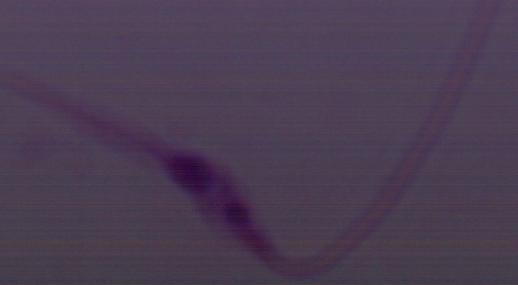

1000x magnification. Micrograph. A Leishmania parasite is shown.